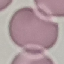
Summary:
  - Result: no malaria parasites seen
  - Preparation: thin blood smear
  - Image type: cell patch, automatically extracted from a larger field of view and resized to 64 × 64 pixels
  - Capture: smartphone through the microscope eyepiece
  - Stain: Giemsa